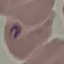
Summary:
  - Malaria status: parasitized
  - Image type: automatically extracted cell patch, resized to 64 × 64 pixels
  - Preparation: thin blood smear
  - Capture: smartphone through the microscope eyepiece
  - Stain: Giemsa